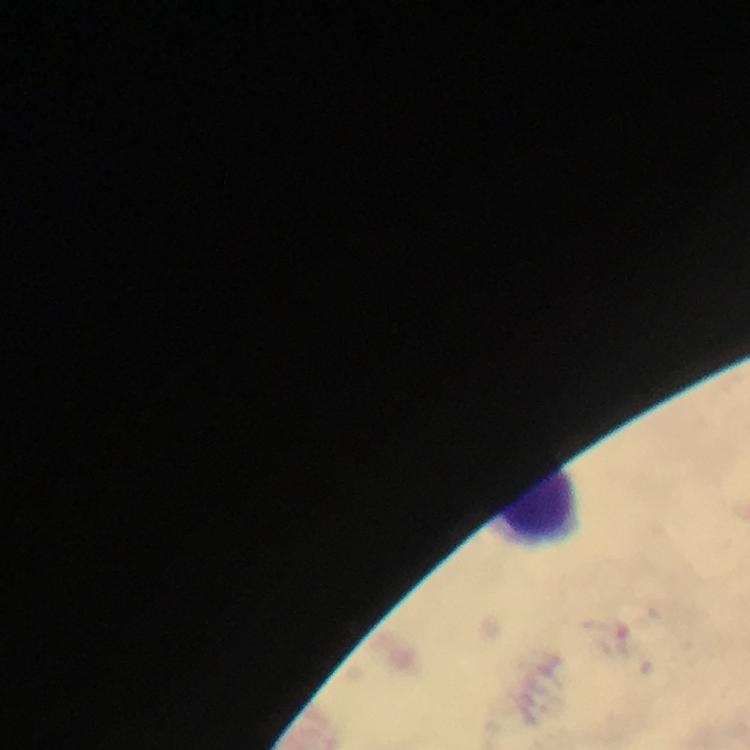

Plasmodium parasites = none detected
image size = 750×750 pixels
magnification = 100x
context = from a diagnostic examination for malaria
leukocyte locations = approximate centers as (x, y) in pixels: (539, 507)
capture = smartphone photograph through a microscope
preparation = thick blood smear
stain = Giemsa
cropped from = a single field of view
immersion oil = applied